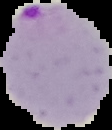
Cell region segmented out of the field of view; the surrounding area is masked to black. Result: malaria parasites identified. Image is 112×130 pixels. From a thin blood smear.